State which parasite is depicted.
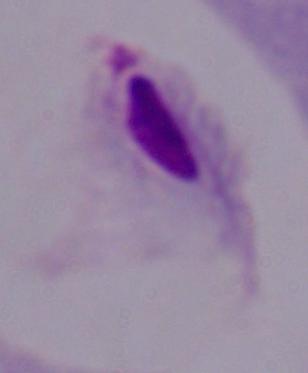
This is a trichomonad.

Summary:
  - Magnification: 1000x
  - Modality: micrograph